Comment on the morphology of the red blood cells.
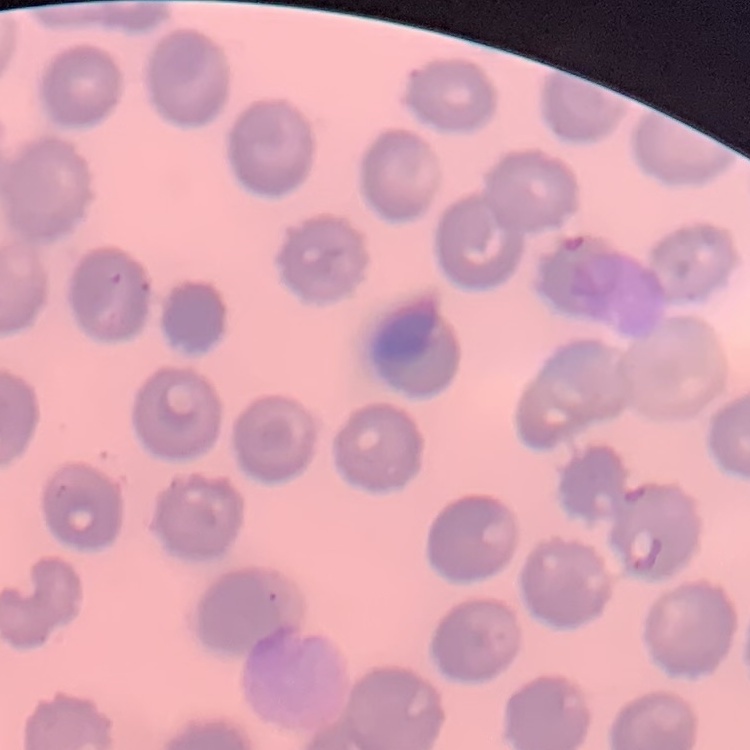

They show no rouleaux formation.

Square crop of a larger photomicrograph. Field's or Giemsa stain. Thin blood film.